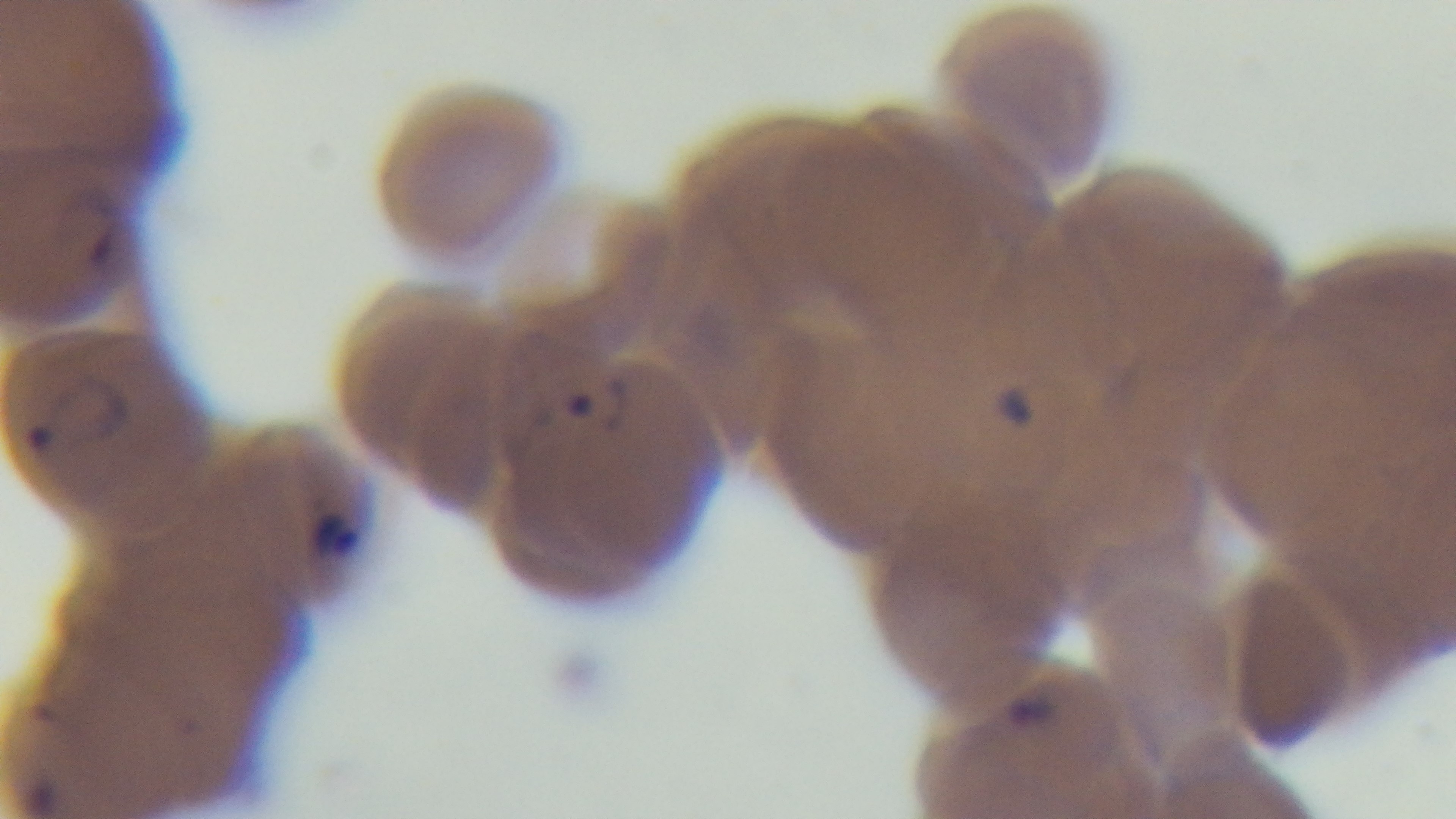
Summary:
  - Objective: 100x oil immersion
  - Stain: Giemsa
  - Malaria status: positive
  - Preparation: thin blood film
  - Field of view: one from the slide
  - Modality: light microscopy
  - Capture: mounted 4K digital camera